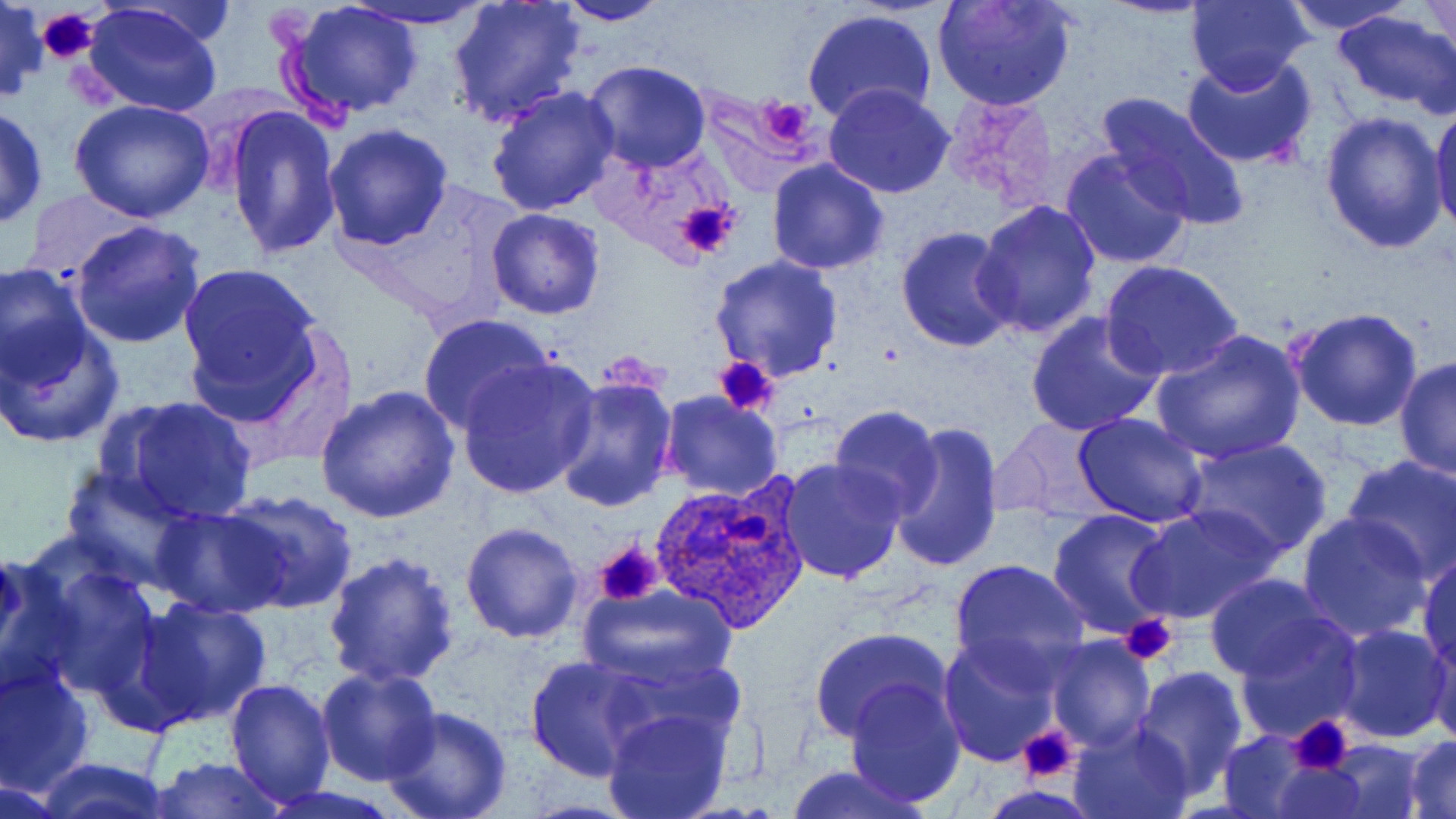
Summary:
  - Coordinate format: approximate bounding boxes as [x1, y1, x2, y2] in pixels
  - Platelet locations: [37, 6, 99, 61], [754, 94, 818, 153], [675, 200, 738, 259], [714, 355, 780, 417], [594, 540, 664, 607], [1119, 613, 1179, 667], [1287, 715, 1356, 778], [1016, 726, 1080, 784]
  - Uninfected red blood cell locations: [0, 0, 49, 105], [80, 0, 225, 116], [281, 0, 424, 120], [339, 0, 498, 31], [931, 0, 1077, 111], [1185, 0, 1312, 94], [1280, 0, 1417, 33], [1421, 0, 1454, 63], [448, 1, 586, 128], [552, 1, 672, 26], [801, 8, 940, 128], [1332, 9, 1456, 113], [1182, 56, 1320, 168], [581, 60, 711, 172], [487, 85, 621, 215], [823, 85, 954, 199], [1094, 90, 1248, 228], [71, 99, 217, 224], [1430, 101, 1456, 237], [0, 105, 48, 229], [225, 105, 342, 259], [1320, 111, 1449, 254], [793, 112, 944, 242], [323, 124, 452, 249], [1061, 148, 1193, 270], [766, 159, 889, 275], [24, 186, 151, 277], [972, 199, 1103, 341], [484, 208, 606, 319], [68, 221, 209, 350], [894, 226, 1017, 352], [711, 256, 843, 381], [177, 259, 331, 417], [1099, 261, 1245, 384], [0, 262, 95, 394], [1289, 307, 1424, 430], [1025, 311, 1165, 436], [417, 313, 554, 432], [0, 325, 124, 449], [1151, 328, 1305, 466], [457, 356, 599, 498], [1394, 357, 1456, 480], [548, 373, 678, 511], [315, 384, 460, 524], [659, 392, 782, 500], [101, 395, 258, 525], [830, 406, 941, 521], [1073, 411, 1209, 528], [993, 417, 1112, 520], [886, 418, 1004, 574], [1182, 436, 1334, 561], [1342, 454, 1456, 580], [777, 458, 907, 585], [61, 467, 196, 589], [219, 487, 361, 613], [150, 503, 287, 619], [1130, 503, 1284, 625], [1046, 509, 1179, 638], [1297, 511, 1433, 641], [460, 521, 584, 644], [1417, 550, 1456, 673], [0, 552, 82, 704], [324, 552, 460, 687], [949, 559, 1090, 681], [32, 562, 162, 700], [1204, 573, 1338, 681], [578, 584, 738, 692], [131, 595, 272, 728], [1235, 617, 1364, 739], [1331, 624, 1453, 743], [807, 627, 955, 746], [1425, 630, 1456, 748], [940, 634, 1063, 766], [1047, 635, 1155, 750], [525, 655, 655, 780], [0, 662, 95, 797], [315, 666, 440, 786], [1133, 666, 1248, 795], [844, 676, 966, 806], [224, 679, 337, 806], [381, 708, 511, 819], [602, 708, 731, 819], [1069, 719, 1196, 819], [1218, 731, 1316, 818], [1403, 736, 1456, 818], [1326, 740, 1424, 818], [145, 755, 289, 818], [31, 758, 176, 818], [1266, 760, 1370, 818], [784, 763, 930, 819], [0, 774, 70, 819]
  - Plasmodium ovale-infected red blood cell locations: [653, 477, 810, 633], [590, 539, 668, 606]
  - Slide-level diagnosis: Plasmodium ovale
  - Image size: 1456×819 pixels
  - Modality: light microscopy
  - Magnification: 1000x
  - Stain: May-Grünwald-Giemsa
  - Field of view: single
  - Preparation: thin blood smear